Assess this cell for malaria.
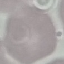

Uninfected.

{
  "stain": "Giemsa",
  "preparation": "thin blood smear",
  "image_type": "automatically extracted cell patch, resized to 64 × 64 pixels",
  "capture": "smartphone camera at the microscope eyepiece"
}